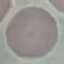

{
  "result": "no malaria parasites seen",
  "stain": "Giemsa",
  "image_type": "automatically extracted cell patch, resized to 64 × 64 pixels",
  "preparation": "thin smear",
  "capture": "smartphone camera at the microscope eyepiece"
}